Name the blood parasite species.
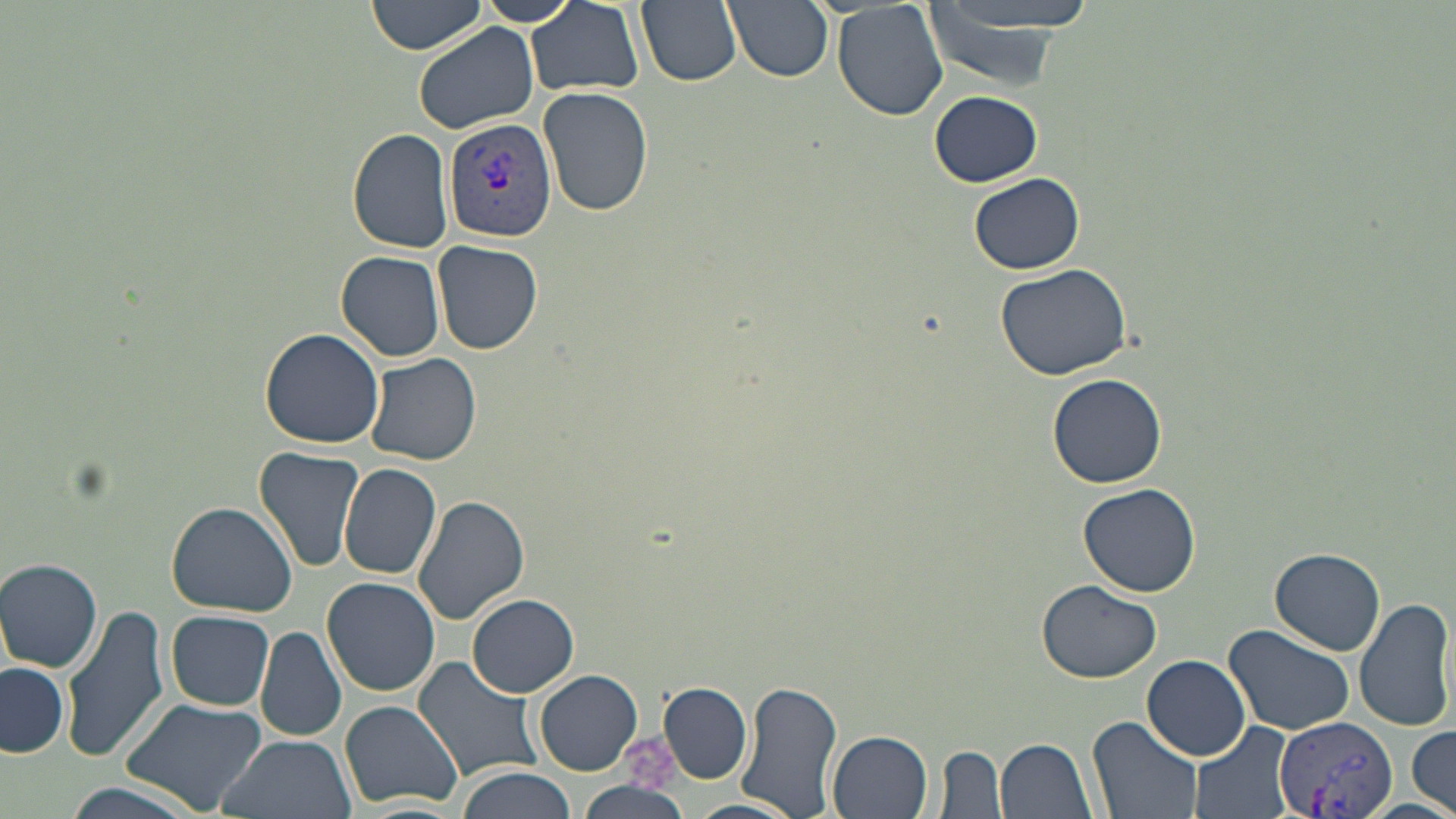

Plasmodium vivax.

Approximate bounding boxes as named x1/y1/x2/y2 corners in pixels. Uninfected red blood cell locations: (x1=367, y1=0, x2=487, y2=55), (x1=471, y1=0, x2=583, y2=28), (x1=636, y1=0, x2=743, y2=87), (x1=723, y1=0, x2=833, y2=83), (x1=924, y1=0, x2=1098, y2=75), (x1=525, y1=1, x2=646, y2=98), (x1=832, y1=1, x2=949, y2=121), (x1=919, y1=1, x2=1110, y2=38), (x1=412, y1=22, x2=539, y2=135), (x1=537, y1=87, x2=654, y2=217), (x1=929, y1=90, x2=1041, y2=187), (x1=349, y1=129, x2=454, y2=254), (x1=968, y1=172, x2=1085, y2=275), (x1=432, y1=240, x2=543, y2=354), (x1=336, y1=250, x2=446, y2=361), (x1=995, y1=263, x2=1136, y2=384), (x1=259, y1=326, x2=385, y2=448), (x1=367, y1=353, x2=482, y2=466), (x1=1048, y1=373, x2=1167, y2=488), (x1=254, y1=447, x2=365, y2=574), (x1=339, y1=463, x2=441, y2=582), (x1=1078, y1=483, x2=1203, y2=598), (x1=411, y1=494, x2=530, y2=625), (x1=166, y1=502, x2=297, y2=617), (x1=1269, y1=546, x2=1386, y2=655), (x1=0, y1=558, x2=104, y2=673), (x1=322, y1=576, x2=440, y2=697), (x1=1035, y1=580, x2=1162, y2=683), (x1=468, y1=593, x2=580, y2=694), (x1=1354, y1=597, x2=1455, y2=732), (x1=60, y1=604, x2=171, y2=764), (x1=166, y1=610, x2=274, y2=710), (x1=1222, y1=623, x2=1355, y2=736), (x1=256, y1=627, x2=346, y2=742), (x1=411, y1=656, x2=546, y2=783), (x1=1143, y1=656, x2=1251, y2=761), (x1=1, y1=663, x2=68, y2=757), (x1=535, y1=669, x2=642, y2=776), (x1=734, y1=680, x2=843, y2=817), (x1=659, y1=682, x2=751, y2=782), (x1=117, y1=696, x2=266, y2=816), (x1=339, y1=701, x2=464, y2=810), (x1=1087, y1=715, x2=1204, y2=819), (x1=1190, y1=719, x2=1300, y2=819), (x1=1409, y1=724, x2=1454, y2=816), (x1=828, y1=730, x2=933, y2=818), (x1=216, y1=732, x2=355, y2=819), (x1=997, y1=737, x2=1098, y2=819), (x1=936, y1=744, x2=1007, y2=817), (x1=458, y1=768, x2=577, y2=819), (x1=54, y1=779, x2=204, y2=819), (x1=576, y1=780, x2=693, y2=819), (x1=684, y1=799, x2=802, y2=819). Plasmodium vivax-infected red blood cell locations: (x1=442, y1=116, x2=558, y2=243), (x1=1274, y1=714, x2=1397, y2=819). Single field of view. Light microscopy. May-Grünwald-Giemsa stain. Thin blood film. Image is 1456×819 pixels. Captured at 1000x magnification.